Assess this cell for malaria.
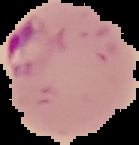
It is parasitized.

From a thin blood smear. Image is 139×145 pixels. The area outside the segmented cell region is set to black.